Classify this cell by malaria status.
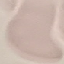
Uninfected.

Summary:
  - Stain: Giemsa
  - Capture: smartphone camera at the microscope eyepiece
  - Image type: cell patch, automatically extracted from a larger field of view and resized to 64 × 64 pixels
  - Preparation: thin blood film